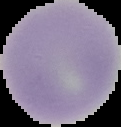 Image is 121×127 pixels. From a thin blood smear. Segmented cell region on a black background. Result: no Plasmodium parasites detected.